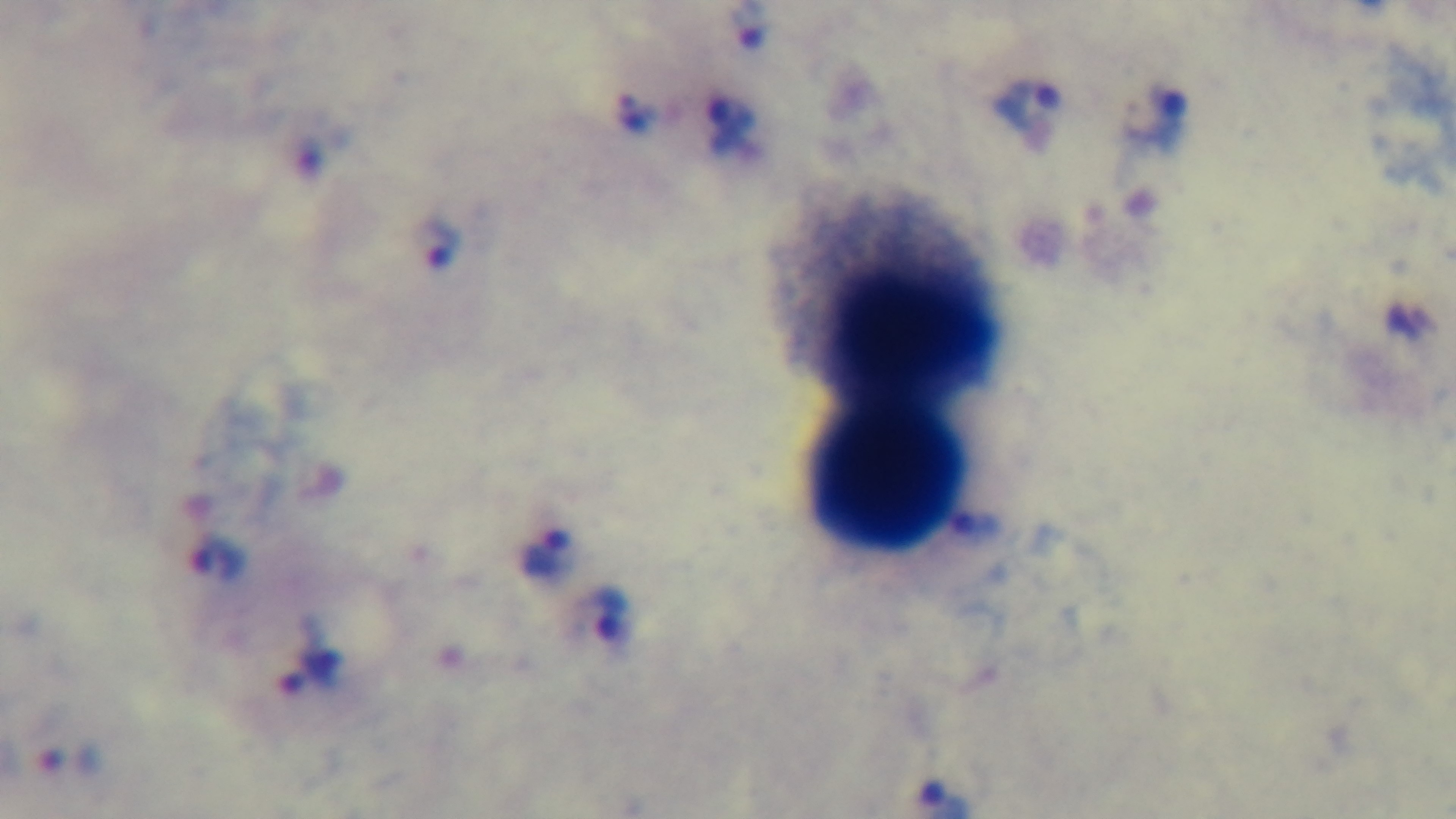
Summary:
  - Stain: Giemsa
  - Modality: light microscopy
  - Preparation: thick blood film
  - Malaria status: positive
  - Capture: mounted 4K digital camera
  - Field of view: single
  - Objective: 100x oil immersion